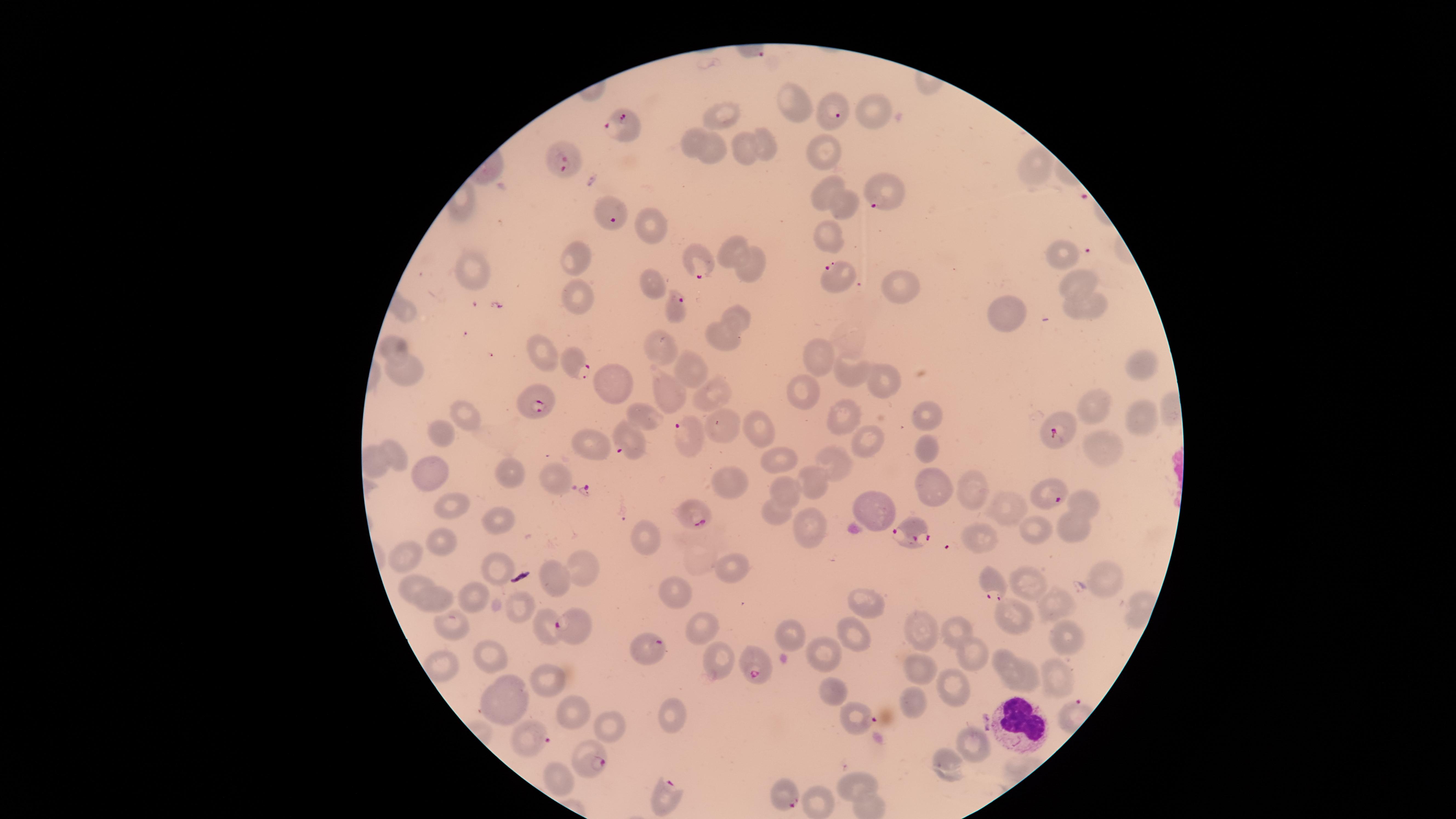
Approximate marker points as [x, y] in pixels. Parasitized RBCs: [837, 116], [626, 127], [566, 158], [884, 198], [609, 212], [695, 260], [839, 277], [675, 311], [577, 363], [534, 405], [1060, 427], [686, 435], [624, 444], [1051, 493], [691, 511], [912, 529], [993, 586], [547, 625], [643, 647], [754, 667], [856, 717], [533, 736], [590, 759], [782, 794], [665, 797]. Uninfected RBCs: [797, 105], [877, 110], [721, 113], [695, 143], [768, 147], [713, 149], [829, 149], [745, 151], [1034, 165], [824, 189], [847, 205], [649, 222], [830, 234], [735, 244], [575, 257], [1067, 258], [753, 267], [476, 278], [1079, 281], [653, 284], [899, 290], [580, 300], [1093, 308], [408, 313], [735, 315], [1005, 318], [724, 336], [395, 347], [661, 349], [544, 356], [822, 360], [1143, 367], [692, 369], [406, 372], [851, 372], [614, 382], [880, 382], [663, 388], [709, 389], [801, 392], [1096, 409], [465, 412], [1143, 414], [841, 415], [647, 417], [923, 417], [724, 421], [759, 431], [446, 434], [595, 443], [864, 443], [1099, 446], [923, 449], [395, 453], [782, 458], [832, 464], [375, 465], [513, 469], [428, 471], [553, 477], [729, 479], [812, 483], [969, 486], [786, 488], [931, 489], [1088, 503], [458, 504], [1004, 508], [874, 510], [774, 513], [504, 516], [808, 523], [1030, 524], [1070, 529], [979, 536], [647, 541], [440, 543], [409, 558], [583, 564], [732, 567], [493, 568], [1105, 576], [558, 577], [1030, 577], [411, 587], [673, 592], [483, 597], [435, 601], [1052, 604], [524, 605], [867, 605], [1016, 615], [451, 625], [577, 628], [699, 629], [922, 629], [956, 629], [790, 633], [851, 637], [1073, 638], [828, 653], [973, 654], [492, 655], [1003, 656], [719, 660], [918, 666], [441, 670], [1027, 676], [552, 679], [1057, 680], [832, 686], [952, 692], [501, 702], [917, 704], [575, 712], [669, 721], [612, 725], [975, 745], [944, 765], [858, 785], [817, 803]. WBCs: [1022, 724]. Presence: malaria parasites seen. Single field of view. Species: Plasmodium falciparum. Photographed with a smartphone camera through the microscope eyepiece. Image is 1456×819 pixels. Giemsa-stained preparation. Thin smear of blood. The visible region is circular.